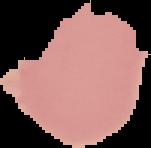
image type = cell region segmented out of the field of view; surrounding area masked to black
result = no Plasmodium parasites detected
image size = 151×148 pixels
preparation = thin blood smear